Assess the morphology of the erythrocytes.
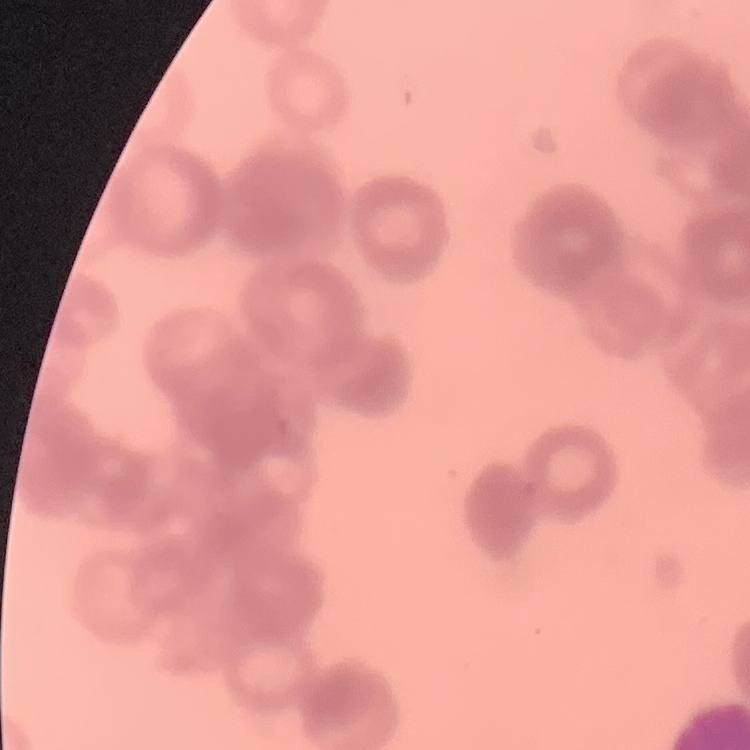
They show rouleaux formation.

Thin blood film. Square crop of a larger photomicrograph. Field's or Giemsa stain.